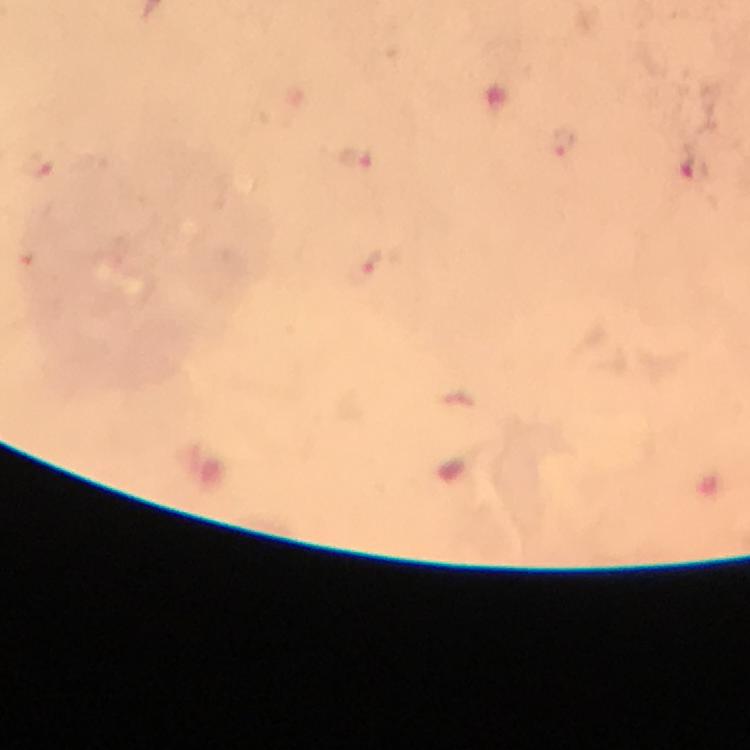

Approximate object centers, in pixels from the top-left corner.
Summary:
  - Plasmodium parasite locations: (x=356, y=160), (x=40, y=166), (x=693, y=169), (x=368, y=262)
  - Magnification: 100x
  - Preparation: thick blood smear
  - Stain: Giemsa
  - Image size: 750×750 pixels
  - Immersion oil: applied
  - Cropped from: a single field of view
  - Capture: smartphone photograph through a microscope
  - Context: from a diagnostic examination for malaria